Classify this cell by malaria status.
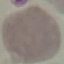

It is uninfected.

Giemsa stain. Acquired by smartphone through the microscope eyepiece. Thin blood smear. Cell patch, automatically extracted from a larger field of view and resized to 64 × 64 pixels.